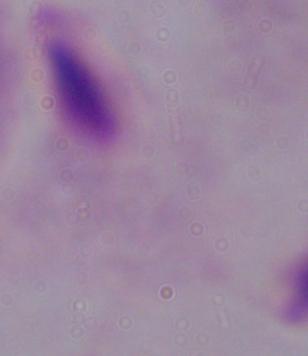
Summary:
  - Modality: micrograph
  - Magnification: 1000x
  - Identification: trichomonad